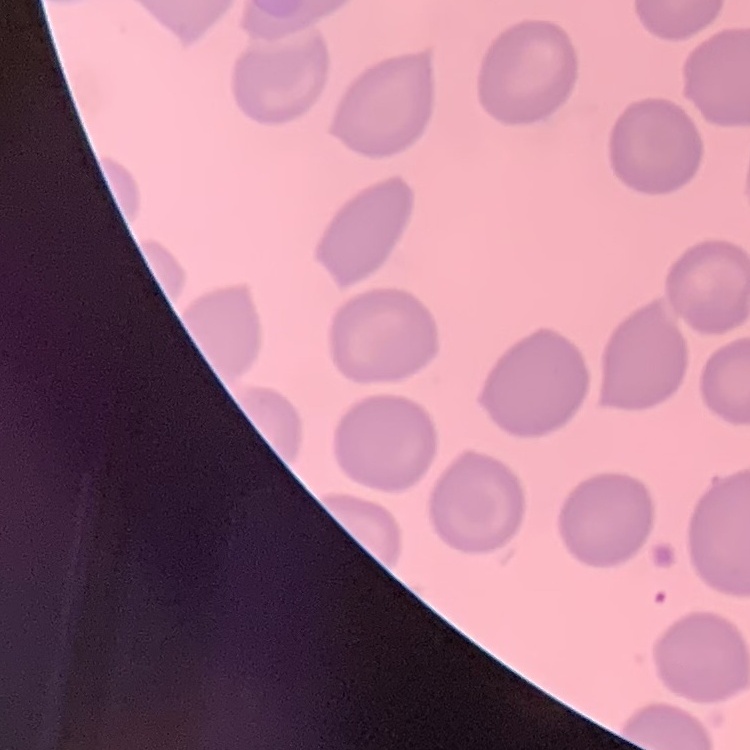

Summary:
  - Erythrocyte morphology: no rouleaux formation
  - Preparation: thin blood smear
  - Image type: one tile cut from a larger photomicrograph
  - Stain: Field's or Giemsa